Give the extent of all Plasmodium falciparum-infected red blood cells.
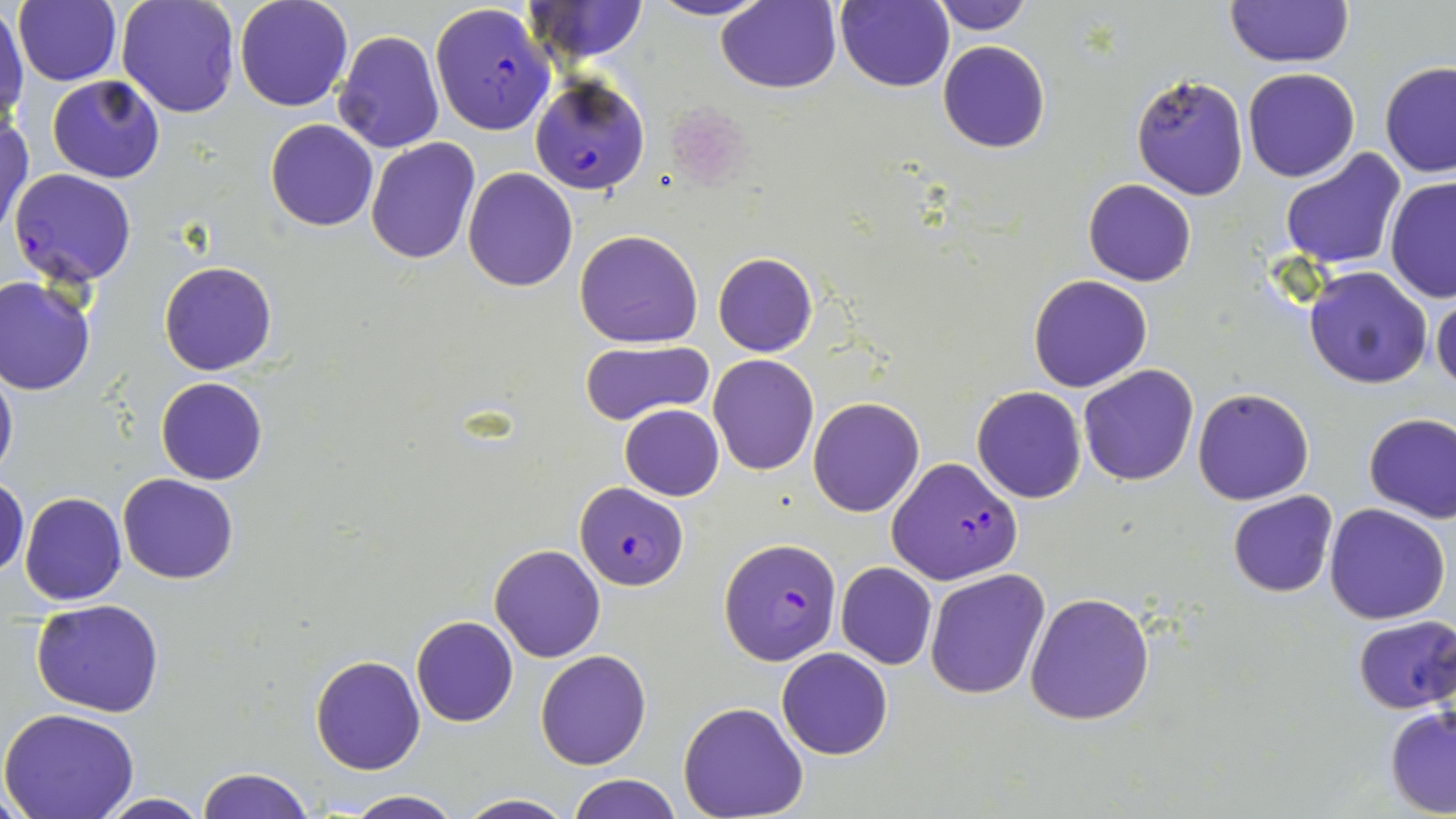

Approximate bounding boxes as named x1/y1/x2/y2 corners in pixels.
Plasmodium falciparum-infected red blood cells: (x1=429, y1=1, x2=555, y2=135), (x1=529, y1=75, x2=651, y2=194), (x1=9, y1=169, x2=139, y2=286), (x1=886, y1=457, x2=1023, y2=586), (x1=573, y1=482, x2=690, y2=590), (x1=718, y1=536, x2=843, y2=665).

Uninfected red blood cell locations: (x1=14, y1=0, x2=121, y2=86), (x1=116, y1=0, x2=239, y2=120), (x1=234, y1=0, x2=353, y2=112), (x1=650, y1=0, x2=769, y2=21), (x1=835, y1=0, x2=954, y2=92), (x1=527, y1=1, x2=649, y2=63), (x1=714, y1=1, x2=841, y2=93), (x1=931, y1=1, x2=1036, y2=34), (x1=1224, y1=1, x2=1354, y2=68), (x1=0, y1=8, x2=26, y2=128), (x1=334, y1=30, x2=443, y2=152), (x1=937, y1=40, x2=1050, y2=154), (x1=1380, y1=62, x2=1456, y2=178), (x1=1243, y1=67, x2=1361, y2=182), (x1=1130, y1=73, x2=1249, y2=202), (x1=47, y1=76, x2=166, y2=184), (x1=1, y1=116, x2=33, y2=237), (x1=265, y1=119, x2=379, y2=231), (x1=366, y1=138, x2=481, y2=264), (x1=1278, y1=148, x2=1407, y2=269), (x1=462, y1=168, x2=579, y2=292), (x1=1385, y1=176, x2=1456, y2=305), (x1=1083, y1=179, x2=1197, y2=286), (x1=575, y1=229, x2=703, y2=348), (x1=713, y1=252, x2=817, y2=357), (x1=159, y1=261, x2=277, y2=376), (x1=1304, y1=265, x2=1434, y2=389), (x1=1027, y1=275, x2=1152, y2=392), (x1=0, y1=276, x2=96, y2=395), (x1=1430, y1=287, x2=1455, y2=396), (x1=579, y1=338, x2=715, y2=426), (x1=708, y1=353, x2=819, y2=474), (x1=0, y1=361, x2=17, y2=486), (x1=1078, y1=364, x2=1199, y2=485), (x1=156, y1=377, x2=268, y2=485), (x1=972, y1=386, x2=1087, y2=503), (x1=1192, y1=387, x2=1314, y2=504), (x1=808, y1=397, x2=925, y2=517), (x1=619, y1=404, x2=724, y2=500), (x1=1363, y1=413, x2=1456, y2=523), (x1=117, y1=474, x2=239, y2=584), (x1=0, y1=476, x2=28, y2=580), (x1=1227, y1=490, x2=1339, y2=597), (x1=17, y1=491, x2=127, y2=606), (x1=1324, y1=502, x2=1451, y2=624), (x1=489, y1=544, x2=605, y2=663), (x1=836, y1=562, x2=937, y2=670), (x1=925, y1=568, x2=1050, y2=699), (x1=1025, y1=592, x2=1154, y2=725), (x1=32, y1=601, x2=164, y2=717), (x1=410, y1=615, x2=519, y2=726), (x1=1351, y1=615, x2=1456, y2=713), (x1=776, y1=647, x2=894, y2=760), (x1=534, y1=649, x2=651, y2=769), (x1=311, y1=654, x2=425, y2=775), (x1=678, y1=701, x2=808, y2=819), (x1=1385, y1=704, x2=1456, y2=817), (x1=1, y1=709, x2=141, y2=819), (x1=198, y1=767, x2=314, y2=819), (x1=569, y1=774, x2=682, y2=819), (x1=344, y1=791, x2=463, y2=819), (x1=96, y1=793, x2=213, y2=818), (x1=457, y1=793, x2=573, y2=819). Slide-level diagnosis: Plasmodium falciparum. May-Grünwald-Giemsa-stained preparation. Thin blood film. Light microscopy. Captured at 1000x magnification. Image is 1456×819 pixels. One field of a larger specimen.